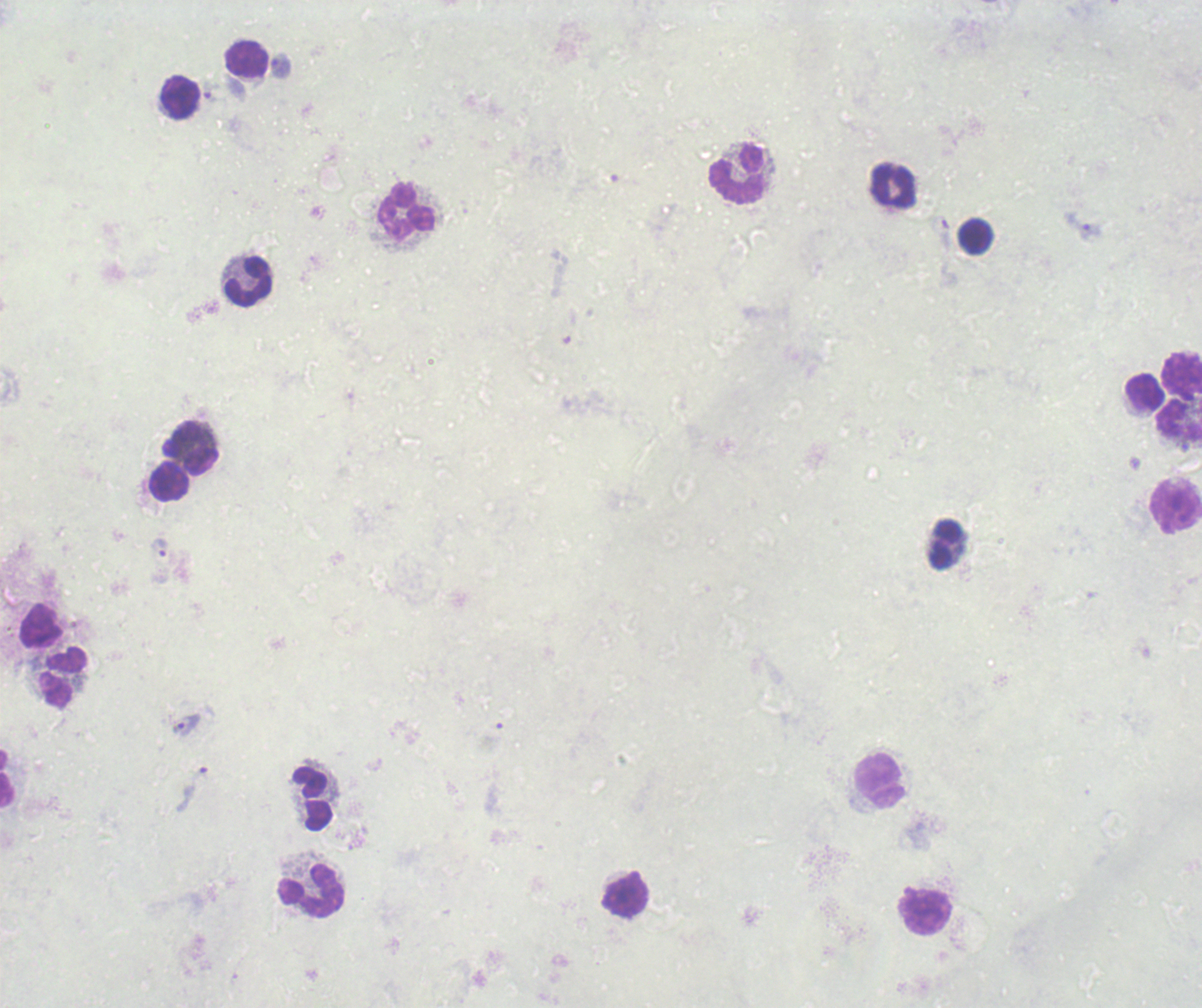

{
  "leukocyte_locations": "approximate object centers, in pixels from the top-left corner: (x=247, y=59), (x=179, y=97), (x=737, y=176), (x=893, y=187), (x=406, y=211), (x=975, y=237), (x=248, y=283), (x=1182, y=374), (x=1145, y=393), (x=1179, y=421), (x=191, y=449), (x=169, y=482), (x=1176, y=504), (x=945, y=546), (x=41, y=626), (x=64, y=677), (x=7, y=780), (x=879, y=781), (x=311, y=799), (x=310, y=891), (x=624, y=895), (x=926, y=912)",
  "preparation": "thick blood film",
  "field_of_view": "single",
  "result": "Plasmodium parasites identified",
  "trophozoite_locations": "approximate object centers, in pixels from the top-left corner: (x=281, y=66), (x=211, y=93), (x=1082, y=226), (x=941, y=232), (x=159, y=548), (x=186, y=724)",
  "context": "previously used in an actual diagnosis",
  "magnification": "100x",
  "background_quality": "poor",
  "image_size": "1202×1008 pixels",
  "stain": "Romanowsky"
}